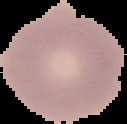

malaria status = uninfected
image type = cell region segmented out of the field of view; surrounding area masked to black
image size = 127×124 pixels
preparation = thin blood smear